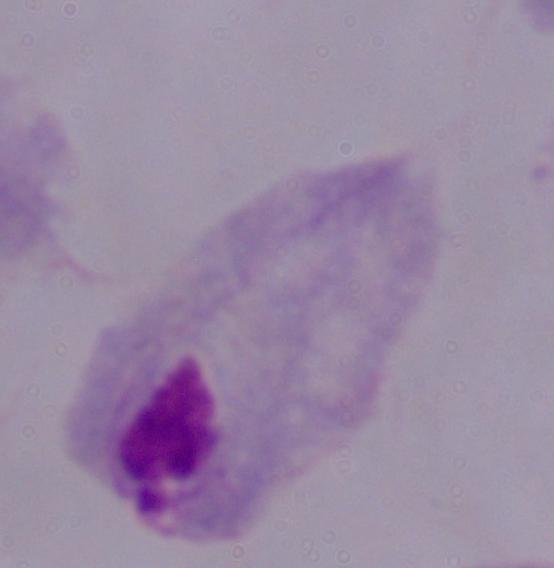
1000x magnification. A trichomonad is seen. Micrograph.